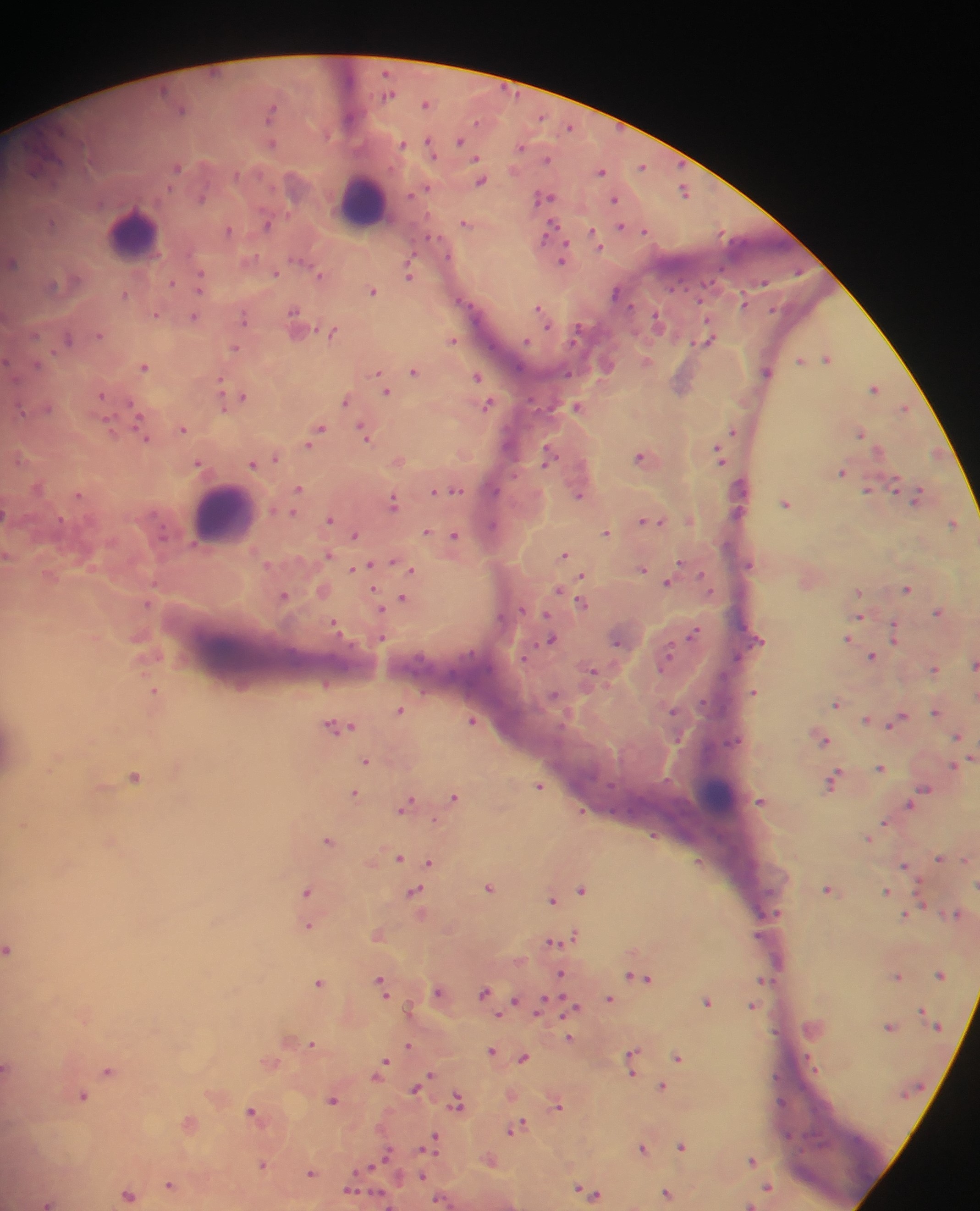
Approximate centers as {x, y} in pixels.
Summary:
  - Leukocyte locations: {360, 202}, {132, 235}, {223, 513}, {722, 797}
  - Plasmodium parasite locations: {385, 72}, {389, 95}, {426, 103}, {182, 108}, {272, 111}, {349, 118}, {570, 127}, {461, 140}, {272, 143}, {429, 143}, {403, 144}, {521, 146}, {477, 159}, {548, 159}, {642, 166}, {178, 168}, {601, 171}, {237, 175}, {481, 181}, {428, 188}, {684, 191}, {411, 194}, {544, 197}, {202, 198}, {615, 200}, {51, 223}, {466, 223}, {268, 224}, {620, 226}, {551, 228}, {644, 230}, {229, 231}, {593, 234}, {433, 238}, {597, 243}, {298, 259}, {563, 259}, {13, 262}, {275, 274}, {319, 274}, {409, 274}, {201, 281}, {762, 282}, {172, 283}, {52, 285}, {373, 291}, {617, 293}, {125, 294}, {463, 301}, {744, 303}, {540, 309}, {295, 310}, {156, 314}, {194, 317}, {245, 317}, {657, 320}, {333, 332}, {577, 333}, {36, 335}, {99, 335}, {68, 338}, {708, 338}, {452, 339}, {235, 348}, {827, 358}, {6, 360}, {801, 360}, {647, 361}, {36, 365}, {607, 365}, {144, 367}, {414, 371}, {766, 372}, {377, 373}, {477, 376}, {220, 382}, {874, 388}, {386, 391}, {102, 395}, {242, 397}, {345, 401}, {488, 404}, {578, 406}, {48, 407}, {223, 407}, {905, 408}, {133, 409}, {21, 412}, {109, 426}, {139, 426}, {321, 428}, {182, 429}, {734, 431}, {366, 434}, {861, 434}, {313, 439}, {146, 440}, {309, 445}, {879, 449}, {937, 453}, {719, 454}, {549, 455}, {640, 457}, {277, 458}, {198, 463}, {253, 464}, {842, 472}, {895, 486}, {300, 488}, {867, 489}, {438, 490}, {456, 491}, {79, 495}, {579, 496}, {918, 496}, {393, 502}, {786, 503}, {293, 512}, {4, 513}, {330, 520}, {642, 521}, {660, 522}, {952, 523}, {493, 524}, {426, 532}, {606, 532}, {354, 535}, {454, 535}, {329, 555}, {565, 555}, {679, 562}, {392, 563}, {369, 565}, {355, 568}, {642, 569}, {412, 570}, {582, 576}, {668, 582}, {906, 588}, {558, 590}, {859, 593}, {284, 595}, {403, 598}, {148, 604}, {583, 604}, {380, 607}, {938, 612}, {547, 614}, {859, 616}, {336, 627}, {894, 631}, {693, 634}, {848, 639}, {382, 640}, {551, 640}, {617, 642}, {873, 657}, {667, 658}, {974, 663}, {935, 669}, {593, 671}, {155, 691}, {754, 692}, {553, 695}, {837, 703}, {400, 710}, {674, 710}, {935, 712}, {866, 719}, {899, 719}, {472, 721}, {893, 723}, {340, 726}, {958, 736}, {825, 741}, {366, 761}, {953, 766}, {880, 767}, {134, 776}, {831, 781}, {539, 786}, {925, 790}, {354, 793}, {453, 796}, {760, 802}, {909, 804}, {406, 805}, {582, 812}, {884, 823}, {653, 836}, {868, 837}, {327, 840}, {399, 858}, {939, 858}, {966, 860}, {430, 862}, {905, 865}, {489, 887}, {582, 889}, {828, 889}, {886, 891}, {307, 892}, {415, 892}, {552, 900}, {957, 914}, {906, 915}, {308, 926}, {571, 936}, {552, 942}, {8, 949}, {941, 974}, {561, 975}, {898, 976}, {641, 977}, {764, 980}, {319, 983}, {382, 983}, {438, 991}, {484, 993}, {609, 999}, {514, 1001}, {707, 1001}, {542, 1006}, {753, 1006}, {573, 1007}, {922, 1010}, {890, 1026}, {569, 1038}, {312, 1043}, {408, 1045}, {491, 1051}, {633, 1057}, {523, 1058}, {679, 1058}, {381, 1067}, {7, 1068}, {108, 1071}, {632, 1073}, {417, 1087}, {662, 1087}, {82, 1096}, {332, 1099}, {459, 1102}, {557, 1106}, {252, 1112}, {516, 1127}, {432, 1142}, {681, 1146}, {642, 1148}, {386, 1155}, {752, 1160}, {262, 1165}, {310, 1173}, {422, 1176}, {170, 1185}, {769, 1187}, {349, 1189}, {579, 1189}, {667, 1193}, {129, 1194}, {595, 1194}, {440, 1200}, {47, 1203}, {751, 1205}
  - Country: Ghana
  - Capture: mobile-phone photograph through a microscope
  - Preparation: thick blood film
  - Field of view: single
  - Image size: 980×1211 pixels